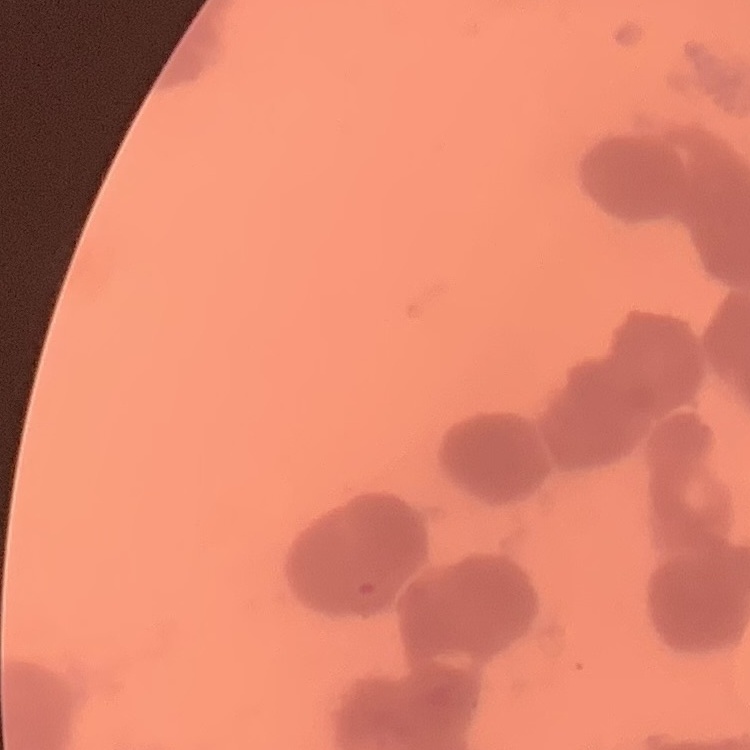 The red blood cells show rouleaux formation. Square crop of a larger photomicrograph. Thin blood smear. Field's or Giemsa stain.